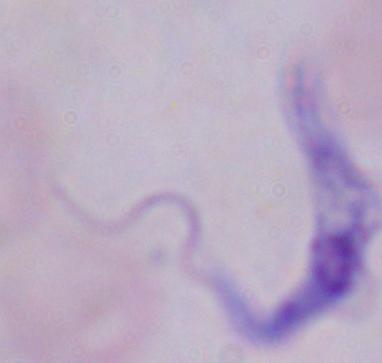
A trypanosome is seen. Photomicrograph. Captured at 1000x magnification.